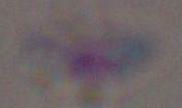
Summary:
  - Magnification: 1000x
  - Identification: Toxoplasma gondii
  - Modality: photomicrograph